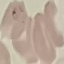
Result: malaria parasites identified. Automatically extracted cell patch, resized to 64 × 64 pixels. Giemsa-stained preparation. Photographed with a smartphone camera at the microscope eyepiece. Thin blood film.